Give the position of every leukocyte visible.
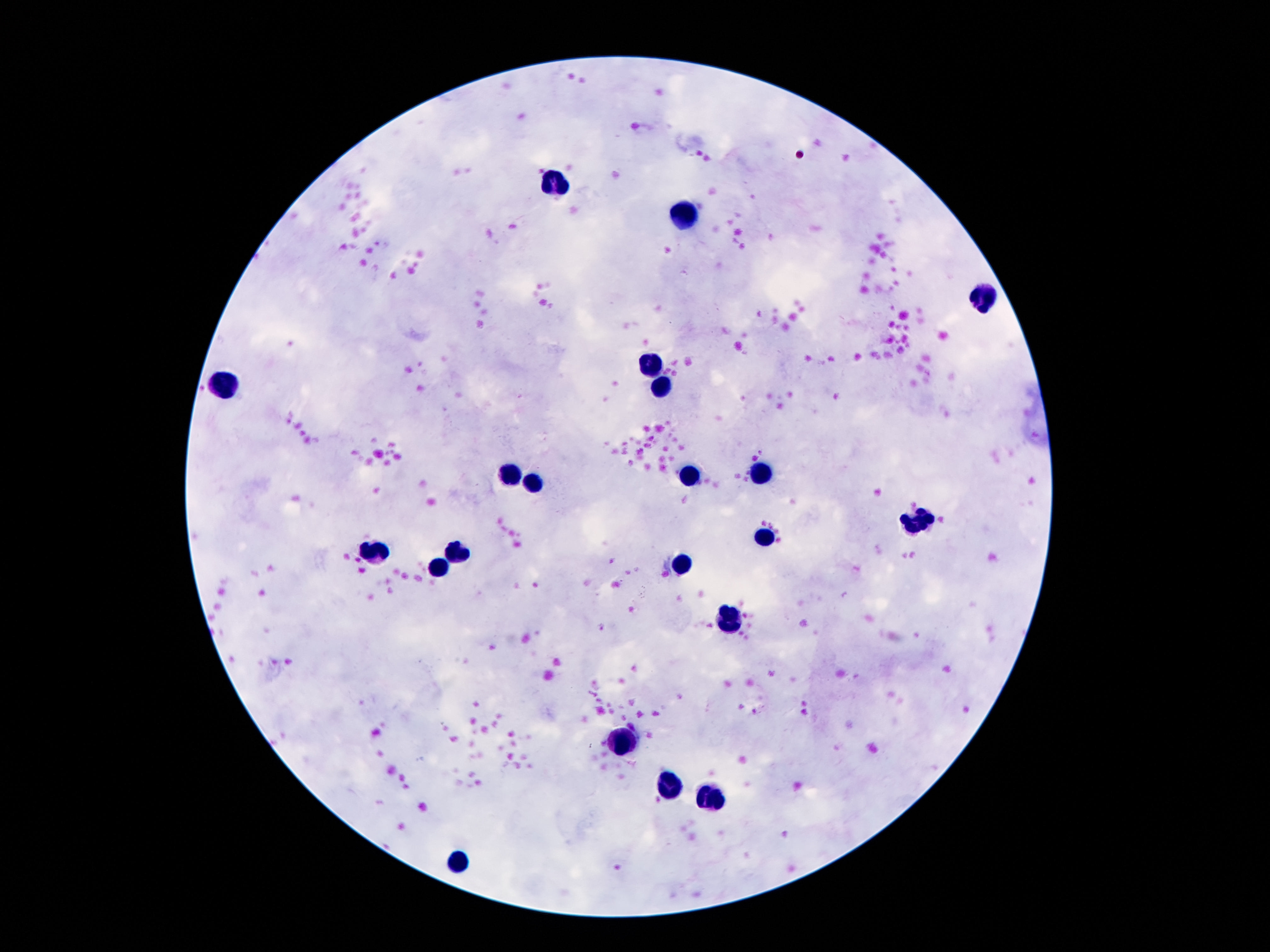
Approximate object centers, in pixels from the top-left corner.
Leukocytes: (x=552, y=181), (x=681, y=220), (x=983, y=297), (x=649, y=367), (x=223, y=380), (x=660, y=388), (x=758, y=472), (x=510, y=476), (x=689, y=476), (x=534, y=481), (x=918, y=521), (x=763, y=535), (x=458, y=551), (x=374, y=556), (x=437, y=566), (x=681, y=567), (x=729, y=621), (x=620, y=741), (x=668, y=787), (x=708, y=796), (x=454, y=864).

{
  "image_size": "1270×952 pixels",
  "field_of_view": "one from this slide",
  "magnification": "100x",
  "preparation": "thick blood film",
  "stain": "Giemsa",
  "patient_malaria_status": "negative",
  "capture": "smartphone camera through the microscope eyepiece"
}